Assess the morphology of the red blood cells.
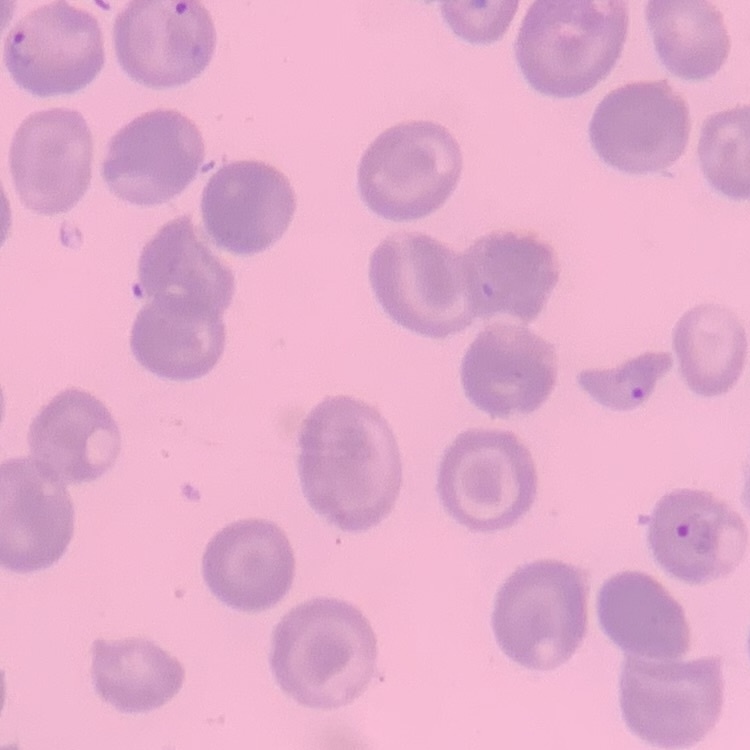

No rouleaux formation.

stain: Field's or Giemsa
preparation: thin peripheral smear
image_type: square crop of a larger photomicrograph